Report the malaria status of this cell.
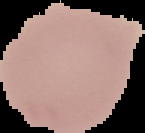
It is uninfected.

image size = 145×133 pixels
preparation = thin blood film
image type = segmented cell region with the area outside set to black